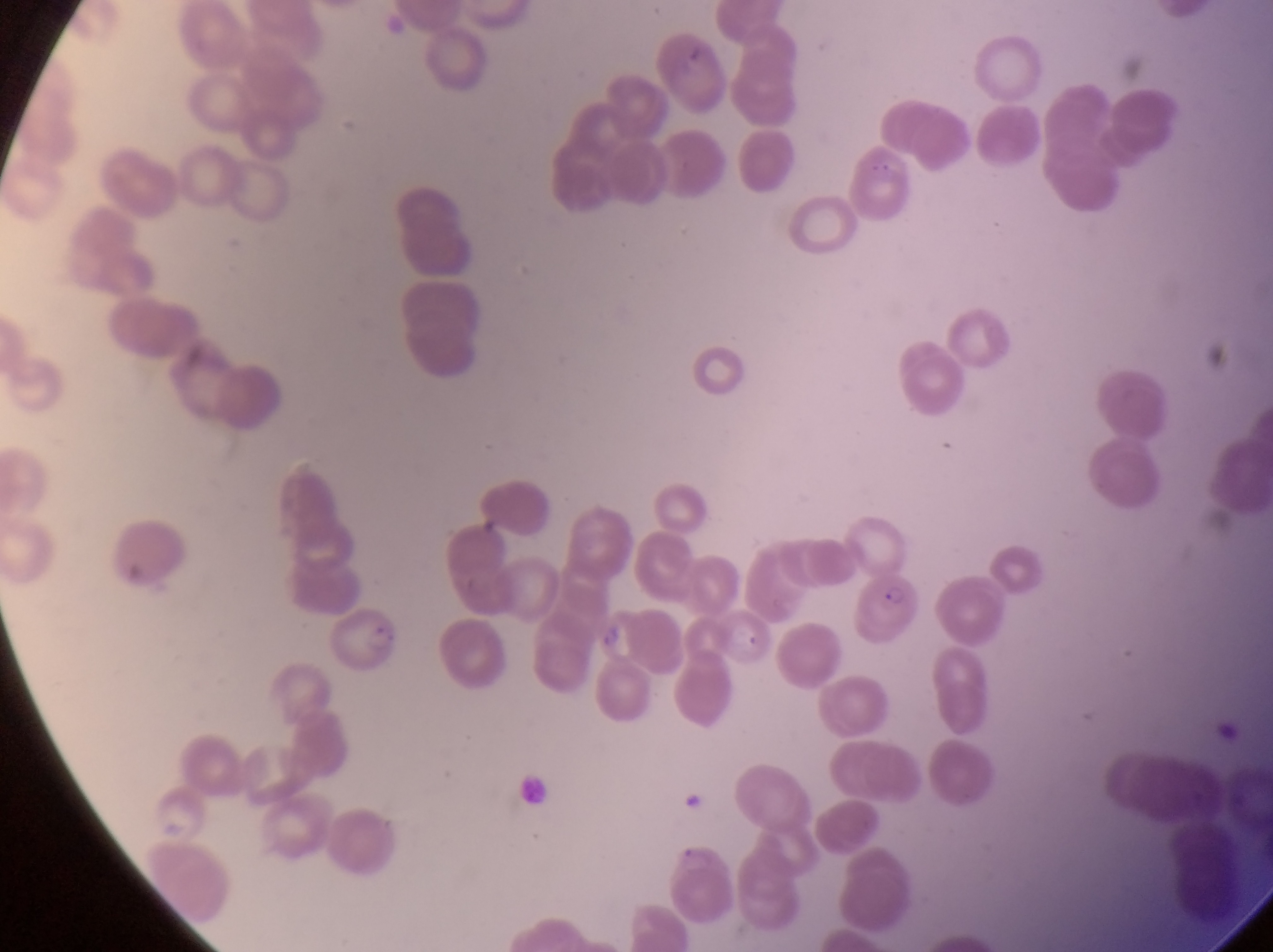
{
  "country": "Uganda",
  "parasitised_red_blood_cell_locations": "approximate bounding boxes as left top right bottom in pixels: 863 569 920 649; 329 604 403 678",
  "image_size": "1273×952 pixels",
  "artifact_platelet_like_body_stain_precipitate_or_debris_locations": "approximate bounding boxes as left top right bottom in pixels: 676 35 718 74; 873 142 905 175; 477 512 505 544",
  "preparation": "thin blood smear",
  "magnification": "1000x",
  "field_of_view": "single",
  "capture": "smartphone photograph through the eyepiece of an Olympus CX-23 microscope"
}